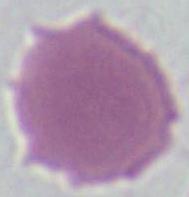

magnification = 1000x
identification = erythrocyte
modality = photomicrograph